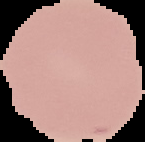

image_type: cell region segmented out of the field of view; surrounding area masked to black
malaria_status: uninfected
preparation: thin blood film
image_size: 145×142 pixels